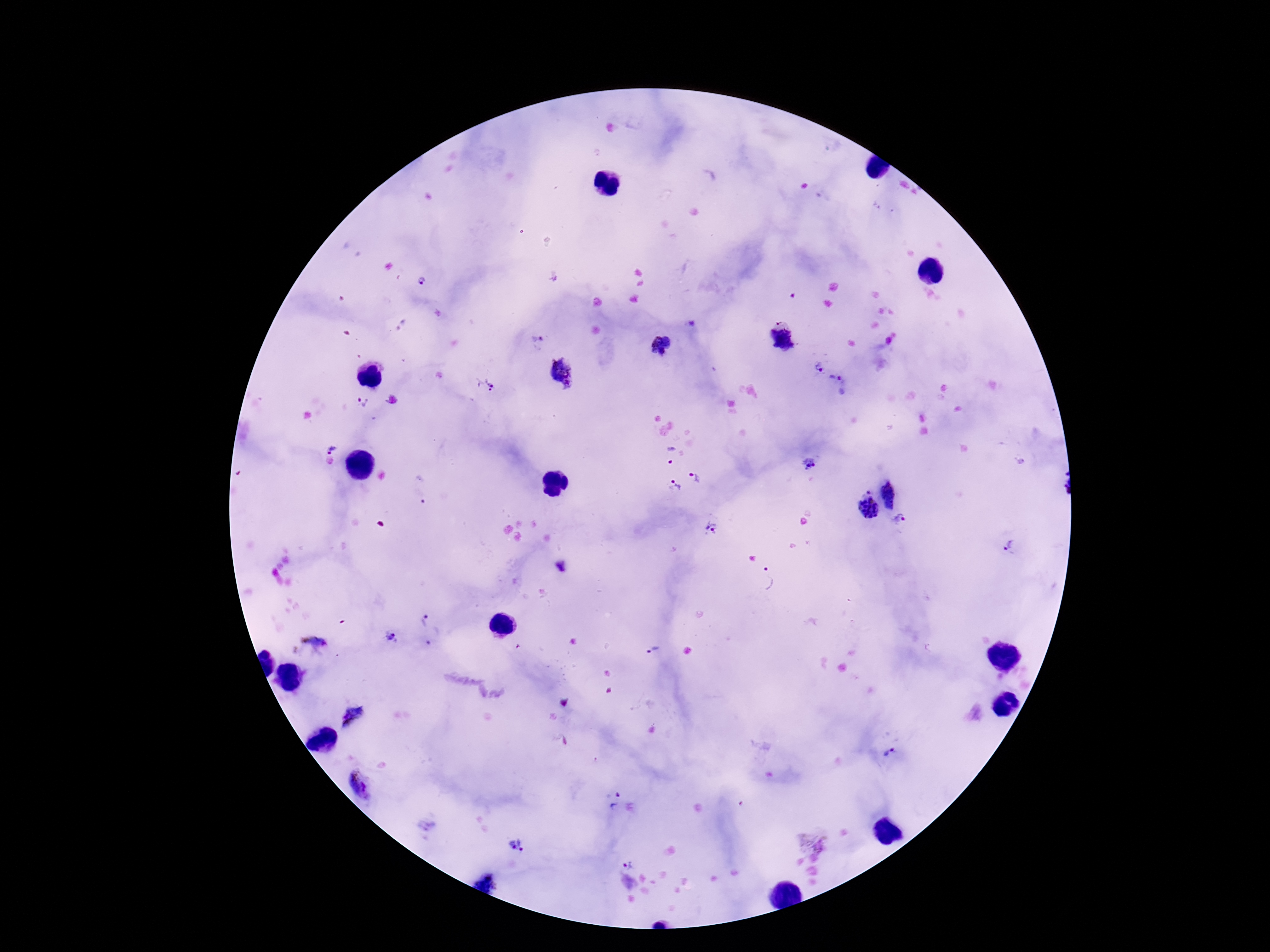

Approximate centers as {x, y} in pixels.
Summary:
  - Plasmodium parasite locations: {421, 282}, {538, 340}, {817, 365}, {560, 371}, {485, 384}, {837, 384}, {362, 403}, {329, 448}, {668, 455}, {810, 463}, {700, 476}, {901, 488}, {674, 490}, {867, 506}, {901, 520}, {712, 529}, {1010, 546}, {562, 567}, {769, 579}, {425, 620}, {434, 637}, {390, 638}, {315, 642}, {654, 650}, {890, 754}, {365, 785}, {614, 801}, {516, 847}, {629, 864}
  - Image size: 1270×952 pixels
  - Preparation: thick blood smear
  - Magnification: 100x
  - Capture: smartphone camera through the microscope eyepiece
  - Patient malaria status: infected
  - Stain: Giemsa
  - Field of view: one from this slide